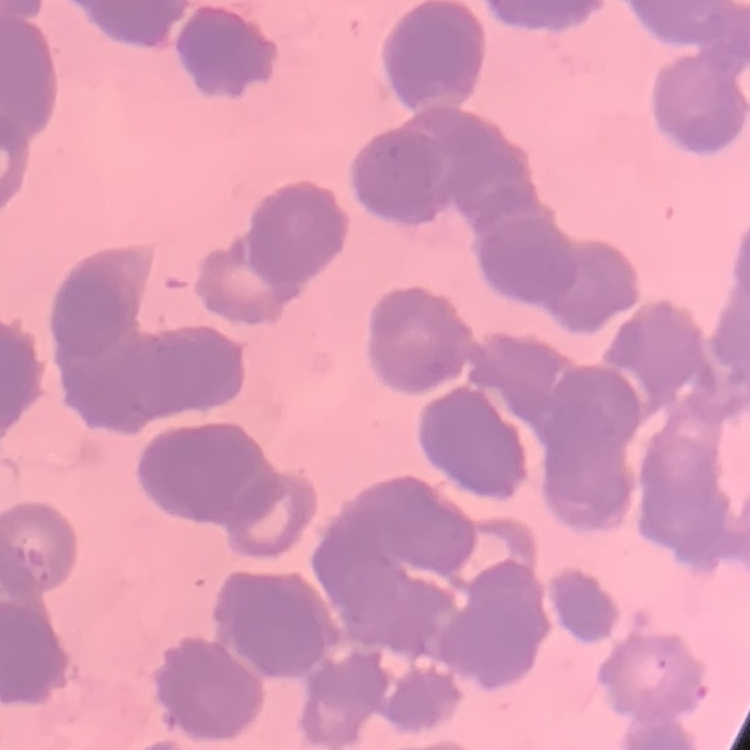
Summary:
  - Red blood cell morphology: rouleaux formation
  - Image type: square crop of a larger photomicrograph
  - Preparation: thin blood smear
  - Stain: Field's or Giemsa